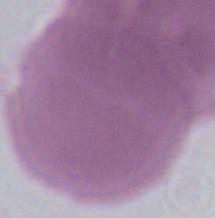
Summary:
  - Modality: photomicrograph
  - Identification: red blood cell
  - Magnification: 1000x